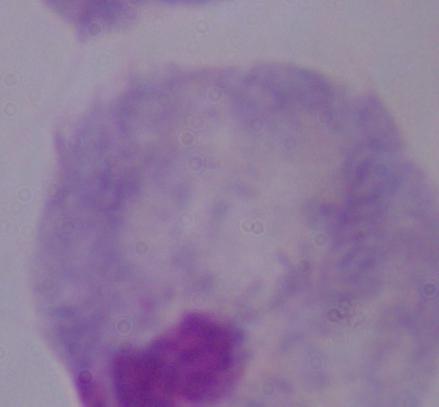

{
  "modality": "micrograph",
  "magnification": "1000x",
  "identification": "trichomonad"
}